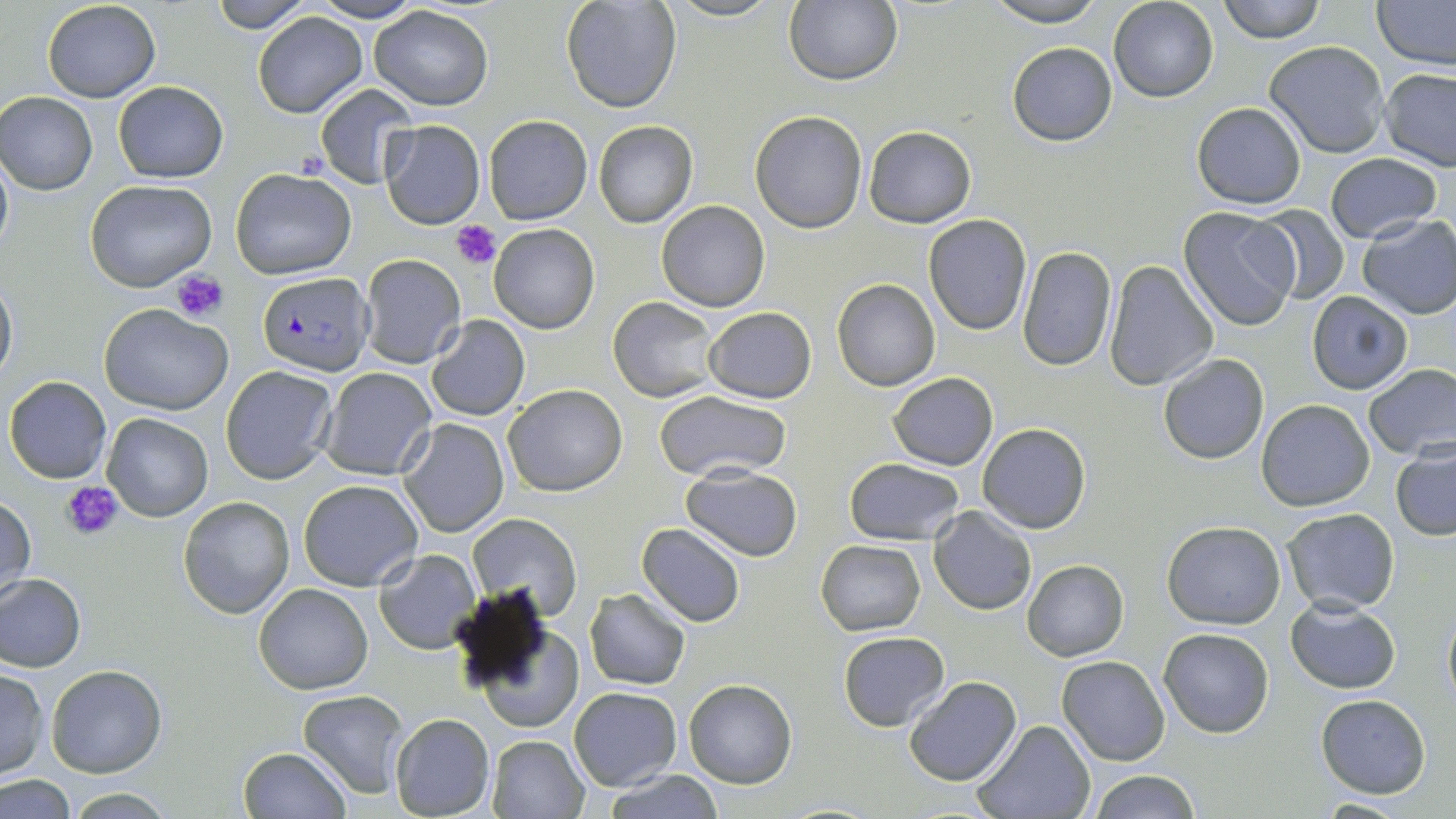
slide-level diagnosis = Plasmodium falciparum
platelet locations = approximate bounding boxes as named x1/y1/x2/y2 corners in pixels: (x1=453, y1=220, x2=501, y2=266), (x1=173, y1=269, x2=229, y2=323), (x1=62, y1=481, x2=126, y2=542)
image size = 1456×819 pixels
stain = May-Grünwald-Giemsa
preparation = thin blood film
Plasmodium falciparum-infected red blood cell locations = approximate bounding boxes as named x1/y1/x2/y2 corners in pixels: (x1=257, y1=271, x2=374, y2=376)
field of view = one of a larger specimen
modality = light microscopy
uninfected red blood cell locations = approximate bounding boxes as named x1/y1/x2/y2 corners in pixels: (x1=42, y1=0, x2=161, y2=102), (x1=208, y1=0, x2=315, y2=32), (x1=308, y1=0, x2=425, y2=23), (x1=559, y1=0, x2=682, y2=113), (x1=663, y1=0, x2=783, y2=22), (x1=787, y1=0, x2=904, y2=85), (x1=981, y1=0, x2=1112, y2=26), (x1=1108, y1=0, x2=1218, y2=102), (x1=1218, y1=0, x2=1325, y2=42), (x1=1376, y1=1, x2=1456, y2=69), (x1=368, y1=6, x2=494, y2=111), (x1=254, y1=10, x2=368, y2=118), (x1=1265, y1=39, x2=1391, y2=159), (x1=1007, y1=42, x2=1117, y2=147), (x1=1379, y1=68, x2=1456, y2=170), (x1=113, y1=81, x2=229, y2=182), (x1=313, y1=84, x2=418, y2=189), (x1=2, y1=92, x2=97, y2=194), (x1=1191, y1=101, x2=1307, y2=209), (x1=750, y1=110, x2=867, y2=232), (x1=483, y1=114, x2=594, y2=224), (x1=380, y1=120, x2=485, y2=229), (x1=592, y1=120, x2=698, y2=228), (x1=864, y1=126, x2=976, y2=226), (x1=0, y1=148, x2=13, y2=264), (x1=1325, y1=152, x2=1443, y2=244), (x1=231, y1=168, x2=356, y2=279), (x1=85, y1=180, x2=218, y2=292), (x1=656, y1=201, x2=771, y2=312), (x1=1252, y1=205, x2=1351, y2=301), (x1=1177, y1=208, x2=1300, y2=332), (x1=923, y1=214, x2=1032, y2=335), (x1=1357, y1=214, x2=1456, y2=320), (x1=488, y1=223, x2=598, y2=334), (x1=1115, y1=232, x2=1267, y2=365), (x1=1018, y1=246, x2=1116, y2=370), (x1=359, y1=254, x2=465, y2=368), (x1=1103, y1=259, x2=1218, y2=392), (x1=0, y1=273, x2=17, y2=387), (x1=832, y1=278, x2=940, y2=391), (x1=1308, y1=291, x2=1413, y2=394), (x1=608, y1=296, x2=719, y2=403), (x1=99, y1=303, x2=234, y2=415), (x1=705, y1=307, x2=816, y2=403), (x1=426, y1=314, x2=530, y2=421), (x1=1156, y1=354, x2=1269, y2=465), (x1=1362, y1=364, x2=1456, y2=461), (x1=220, y1=366, x2=339, y2=483), (x1=318, y1=367, x2=437, y2=480), (x1=888, y1=372, x2=998, y2=470), (x1=4, y1=375, x2=111, y2=484), (x1=503, y1=384, x2=627, y2=496), (x1=651, y1=391, x2=794, y2=484), (x1=1256, y1=399, x2=1376, y2=512), (x1=102, y1=413, x2=213, y2=522), (x1=398, y1=419, x2=510, y2=537), (x1=977, y1=423, x2=1090, y2=533), (x1=1391, y1=445, x2=1456, y2=541), (x1=844, y1=458, x2=965, y2=545), (x1=681, y1=465, x2=803, y2=560), (x1=299, y1=478, x2=423, y2=590), (x1=1, y1=493, x2=35, y2=603), (x1=179, y1=496, x2=295, y2=618), (x1=929, y1=507, x2=1036, y2=615), (x1=1280, y1=507, x2=1400, y2=614), (x1=466, y1=513, x2=581, y2=622), (x1=1162, y1=520, x2=1286, y2=629), (x1=638, y1=523, x2=745, y2=627), (x1=815, y1=539, x2=926, y2=636), (x1=374, y1=549, x2=480, y2=654), (x1=1022, y1=559, x2=1128, y2=661), (x1=0, y1=574, x2=86, y2=671), (x1=253, y1=583, x2=375, y2=695), (x1=448, y1=586, x2=562, y2=698), (x1=585, y1=588, x2=690, y2=689), (x1=1285, y1=595, x2=1401, y2=695), (x1=1442, y1=605, x2=1456, y2=707), (x1=1157, y1=627, x2=1274, y2=738), (x1=481, y1=628, x2=582, y2=732), (x1=838, y1=631, x2=950, y2=731), (x1=1057, y1=656, x2=1171, y2=766), (x1=45, y1=665, x2=166, y2=777), (x1=0, y1=668, x2=49, y2=778), (x1=903, y1=676, x2=1020, y2=787), (x1=683, y1=678, x2=798, y2=788), (x1=569, y1=687, x2=681, y2=790), (x1=298, y1=691, x2=409, y2=798), (x1=1314, y1=694, x2=1432, y2=797), (x1=389, y1=713, x2=496, y2=818), (x1=973, y1=720, x2=1096, y2=819), (x1=486, y1=735, x2=591, y2=819), (x1=237, y1=747, x2=351, y2=818), (x1=605, y1=770, x2=724, y2=819), (x1=1088, y1=770, x2=1200, y2=819), (x1=0, y1=775, x2=76, y2=817), (x1=64, y1=790, x2=179, y2=819), (x1=1309, y1=796, x2=1416, y2=817)
magnification = 1000x